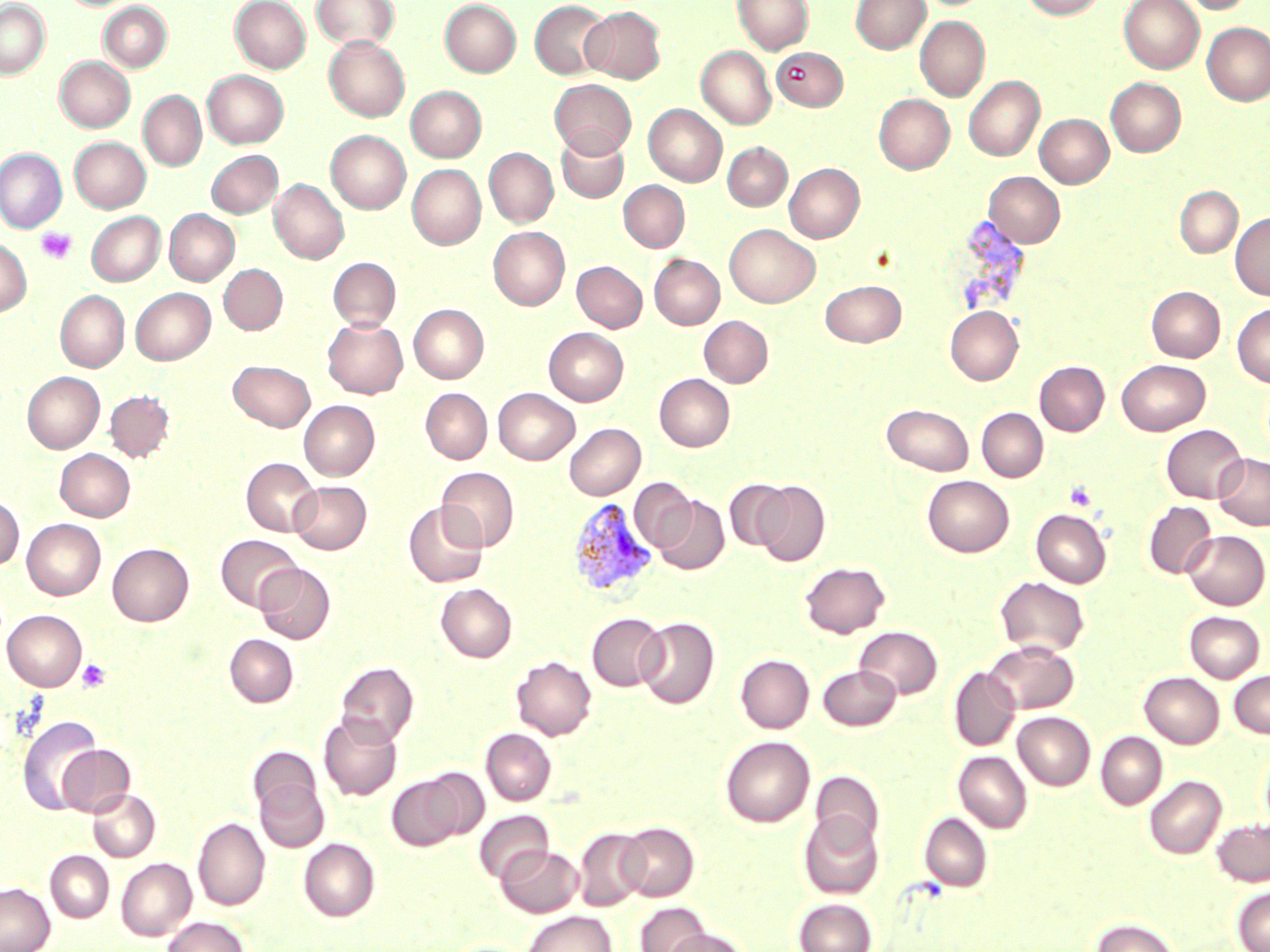

{
  "slide_level_diagnosis": "Plasmodium vivax",
  "stain": "May-Grünwald-Giemsa",
  "field_of_view": "single",
  "plasmodium_vivax_infected_red_blood_cell_locations": "approximate bounding boxes as [x1, y1, x2, y2] in pixels: [567, 498, 659, 597]",
  "platelet_locations": "approximate bounding boxes as [x1, y1, x2, y2] in pixels: [36, 227, 77, 265], [1064, 480, 1097, 511], [77, 659, 112, 693]",
  "modality": "light microscopy",
  "image_size": "1270×952 pixels",
  "preparation": "thin blood film",
  "magnification": "1000x",
  "uninfected_red_blood_cell_locations": "approximate bounding boxes as [x1, y1, x2, y2] in pixels: [62, 0, 135, 10], [230, 0, 310, 73], [311, 0, 399, 51], [733, 0, 813, 54], [851, 0, 930, 53], [1021, 0, 1106, 19], [1119, 0, 1204, 73], [1180, 0, 1253, 14], [0, 1, 49, 79], [440, 1, 521, 76], [530, 1, 611, 79], [99, 2, 172, 73], [581, 6, 665, 83], [915, 16, 989, 101], [1202, 22, 1270, 106], [324, 35, 410, 122], [696, 46, 775, 129], [773, 47, 847, 111], [55, 56, 134, 132], [203, 70, 288, 148], [964, 76, 1044, 161], [1106, 78, 1186, 156], [550, 79, 636, 157], [406, 86, 486, 162], [138, 90, 206, 172], [875, 94, 954, 174], [644, 104, 726, 186], [1035, 114, 1114, 187], [326, 130, 410, 214], [556, 131, 628, 203], [70, 137, 150, 212], [722, 143, 792, 210], [0, 147, 64, 231], [484, 148, 558, 227], [206, 150, 283, 218], [784, 163, 864, 242], [407, 164, 486, 249], [984, 172, 1065, 247], [269, 179, 348, 264], [618, 180, 689, 252], [1175, 186, 1242, 257], [165, 209, 239, 286], [86, 212, 164, 286], [1230, 212, 1270, 301], [725, 224, 820, 307], [488, 227, 569, 309], [0, 240, 31, 316], [650, 254, 725, 329], [328, 258, 400, 331], [572, 261, 647, 332], [219, 264, 287, 334], [820, 280, 906, 347], [1147, 286, 1225, 362], [130, 288, 214, 364], [56, 290, 129, 371], [1233, 303, 1270, 387], [409, 304, 488, 383], [945, 306, 1023, 384], [699, 316, 773, 387], [322, 317, 408, 398], [544, 328, 628, 405], [1117, 359, 1210, 435], [229, 360, 315, 431], [1035, 361, 1109, 435], [23, 372, 104, 453], [654, 374, 734, 451], [421, 388, 492, 464], [493, 388, 579, 464], [105, 390, 174, 462], [299, 401, 379, 480], [882, 403, 974, 476], [977, 408, 1048, 481], [564, 423, 645, 500], [1162, 424, 1247, 502], [55, 449, 135, 521], [1214, 453, 1270, 530], [242, 457, 321, 537], [437, 467, 519, 551], [923, 475, 1013, 556], [630, 478, 696, 551], [724, 479, 792, 553], [290, 481, 371, 554], [754, 481, 830, 566], [0, 495, 24, 570], [654, 496, 729, 574], [404, 501, 488, 588], [1144, 501, 1216, 579], [1031, 509, 1111, 587], [22, 519, 105, 599], [1182, 530, 1269, 609], [217, 534, 301, 612], [107, 543, 193, 626], [799, 561, 890, 638], [255, 563, 335, 644], [995, 577, 1089, 657], [436, 583, 517, 662], [2, 610, 87, 690], [1185, 611, 1265, 682], [587, 612, 666, 691], [636, 617, 719, 709], [854, 627, 942, 699], [224, 634, 298, 707], [985, 641, 1079, 713], [735, 655, 814, 733], [511, 656, 596, 740], [335, 661, 418, 746], [818, 665, 901, 731], [949, 667, 1020, 751], [1229, 669, 1270, 738], [1139, 672, 1224, 748], [319, 712, 402, 801], [1013, 712, 1095, 789], [17, 716, 102, 815], [481, 728, 556, 805], [1096, 732, 1167, 809], [720, 736, 815, 827], [57, 744, 135, 817], [1260, 744, 1270, 832], [248, 746, 322, 820], [954, 751, 1032, 833], [810, 769, 884, 852], [386, 771, 476, 851], [254, 775, 329, 852], [1145, 775, 1226, 858], [87, 788, 160, 861], [474, 810, 553, 883], [919, 812, 993, 891], [799, 813, 884, 899], [193, 818, 270, 910], [1212, 818, 1270, 886], [617, 823, 698, 901], [574, 828, 650, 910], [299, 838, 380, 921], [497, 845, 583, 917], [45, 851, 113, 922], [116, 858, 196, 940], [0, 883, 54, 952], [1233, 887, 1270, 951], [793, 898, 876, 952], [635, 902, 709, 952], [523, 911, 616, 952], [162, 916, 251, 952], [1090, 918, 1179, 952], [664, 928, 749, 952]"
}